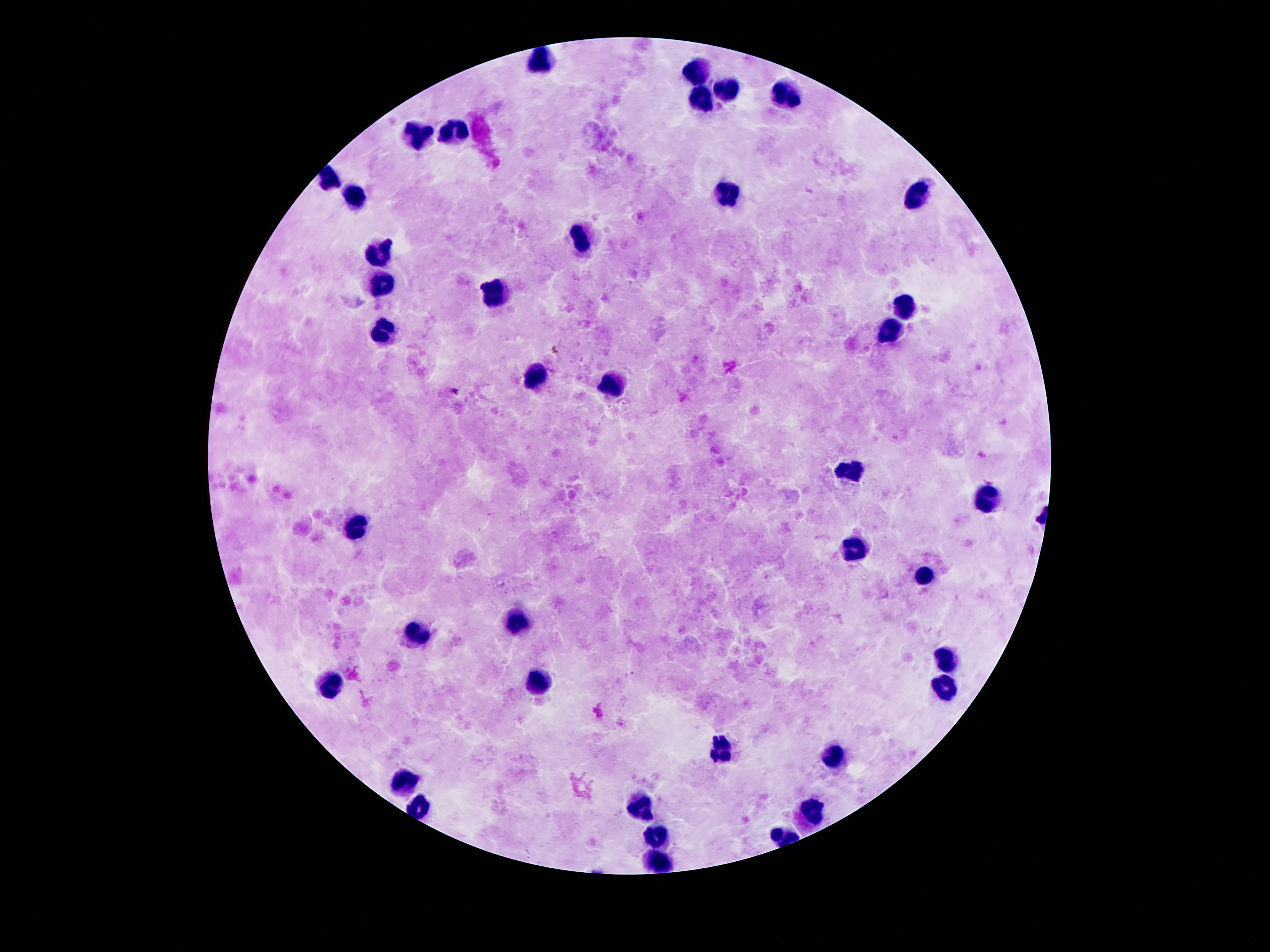

patient malaria status = uninfected
preparation = thick blood smear
stain = Giemsa
leukocyte locations = approximate centers as (x, y) in pixels: (544, 58), (697, 71), (729, 91), (786, 95), (701, 100), (453, 132), (414, 137), (330, 175), (727, 194), (913, 194), (355, 198), (580, 239), (381, 254), (383, 282), (498, 293), (902, 306), (888, 329), (383, 334), (533, 372), (612, 385), (850, 469), (984, 500), (358, 525), (852, 550), (925, 576), (521, 622), (419, 632), (948, 662), (332, 680), (541, 682), (943, 688), (722, 751), (836, 754), (404, 780), (640, 805), (816, 808), (419, 810), (658, 840), (658, 861)
image size = 1270×952 pixels
field of view = single
capture = smartphone camera through the microscope eyepiece
magnification = 100x